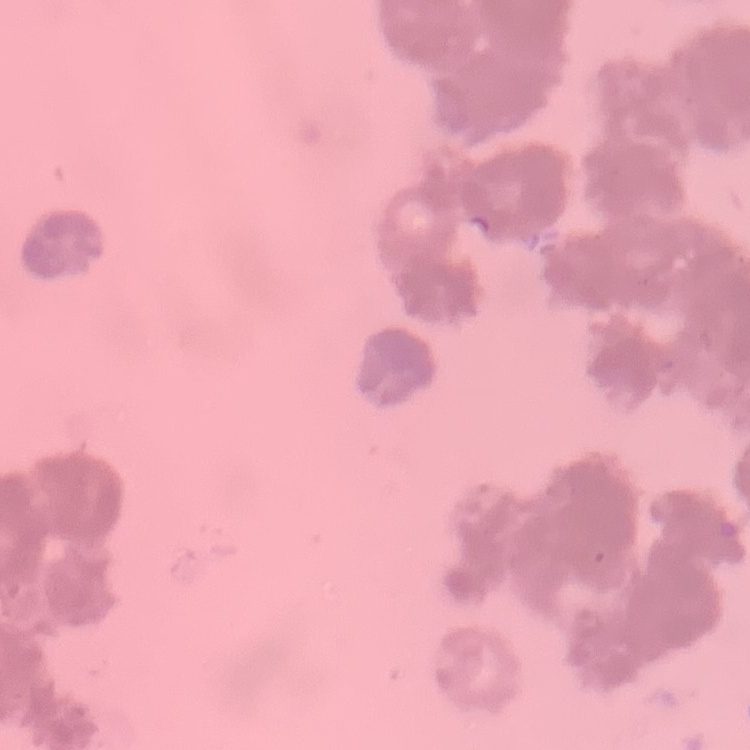

erythrocyte morphology = rouleaux formation
stain = Field's or Giemsa
image type = square crop of a larger photomicrograph
preparation = thin blood smear